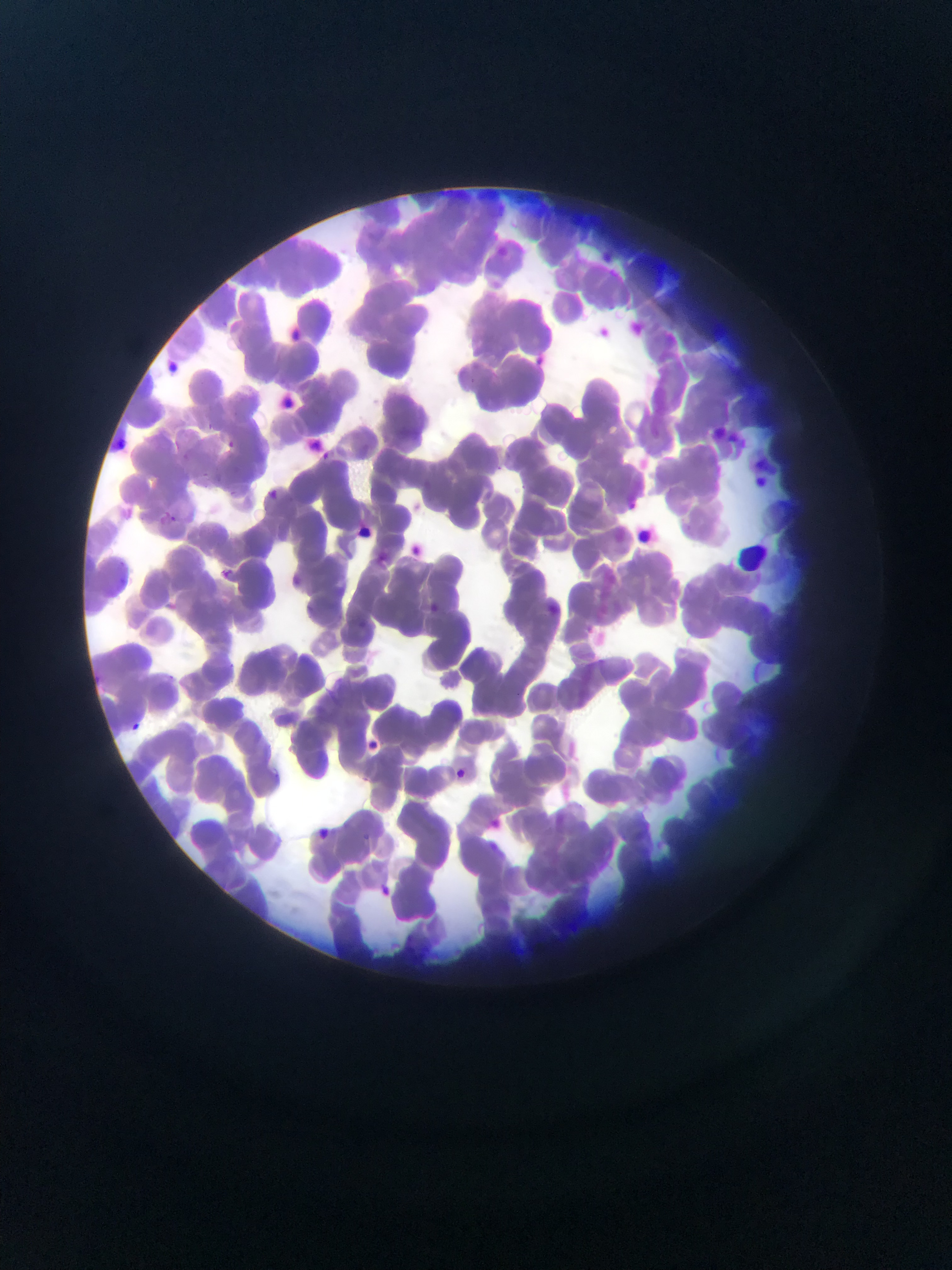

Approximate bounding boxes as [left, top, right, bottom] in pixels. Malaria parasite locations: [537, 348, 548, 366], [164, 360, 186, 381], [222, 437, 237, 451], [311, 446, 332, 463], [195, 469, 212, 484], [223, 487, 239, 500], [265, 487, 281, 501], [409, 498, 426, 512], [157, 511, 178, 529], [407, 542, 427, 560], [375, 551, 393, 566], [217, 566, 233, 581], [288, 569, 303, 587], [430, 600, 440, 615], [306, 602, 318, 616], [357, 617, 369, 632], [126, 719, 143, 736], [364, 740, 386, 753], [449, 766, 469, 785], [482, 813, 505, 841], [311, 826, 332, 844], [372, 880, 396, 901]. Thin blood smear. Collected in Ghana. One field of view. Photographed through a microscope with a mobile-phone camera. Image is 952×1270 pixels.